Identify the parasite.
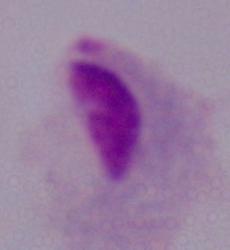
A trichomonad.

1000x magnification. Photomicrograph.